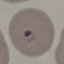 Result: malaria parasites detected. Cell patch, automatically extracted from a larger field of view and resized to 64 × 64 pixels. Giemsa-stained preparation. Thin smear of blood. Acquired by smartphone through the microscope eyepiece.